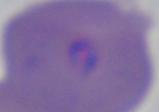
identification: Babesia
magnification: 1000x
modality: micrograph